Report the malaria status of this cell.
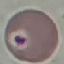
Uninfected.

stain = Giemsa
preparation = thin blood smear
capture = smartphone camera at the microscope eyepiece
image type = automatically extracted cell patch, resized to 64 × 64 pixels